Outline each Plasmodium ovale-infected red blood cell.
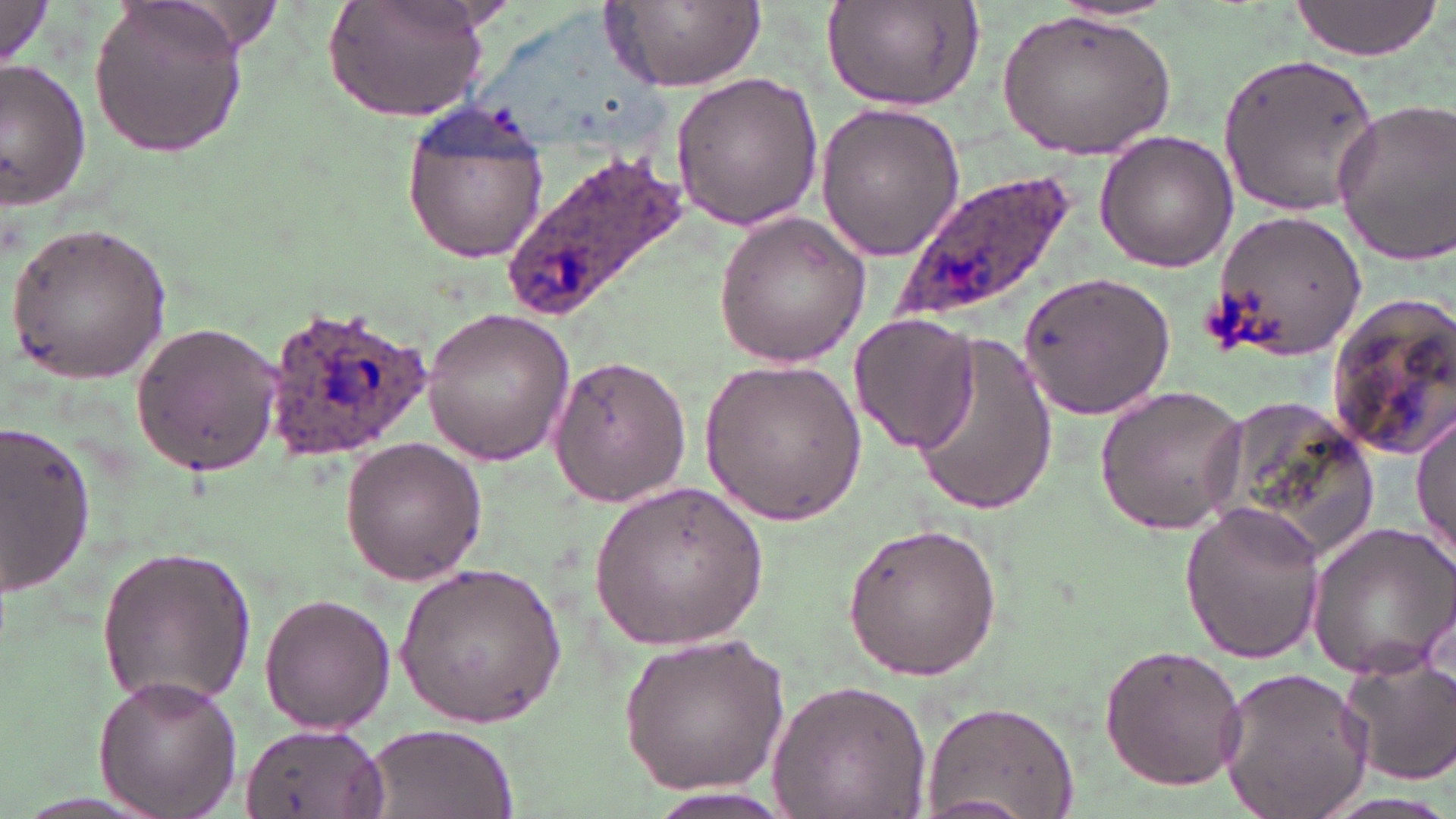
Approximate bounding boxes as named x1/y1/x2/y2 corners in pixels.
Plasmodium ovale-infected red blood cells: (x1=501, y1=145, x2=695, y2=321), (x1=897, y1=169, x2=1083, y2=323), (x1=265, y1=304, x2=434, y2=457).

Uninfected red blood cell locations: (x1=87, y1=0, x2=247, y2=160), (x1=323, y1=0, x2=492, y2=120), (x1=603, y1=0, x2=766, y2=92), (x1=1283, y1=0, x2=1445, y2=60), (x1=0, y1=2, x2=57, y2=72), (x1=821, y1=2, x2=985, y2=113), (x1=997, y1=10, x2=1176, y2=160), (x1=1216, y1=52, x2=1382, y2=215), (x1=0, y1=58, x2=92, y2=210), (x1=669, y1=70, x2=823, y2=231), (x1=1328, y1=97, x2=1456, y2=268), (x1=400, y1=101, x2=554, y2=266), (x1=813, y1=101, x2=967, y2=263), (x1=1093, y1=131, x2=1239, y2=273), (x1=1210, y1=209, x2=1368, y2=363), (x1=712, y1=211, x2=874, y2=368), (x1=5, y1=219, x2=171, y2=384), (x1=1017, y1=271, x2=1175, y2=422), (x1=1322, y1=292, x2=1456, y2=463), (x1=419, y1=306, x2=578, y2=465), (x1=849, y1=314, x2=980, y2=452), (x1=128, y1=320, x2=284, y2=479), (x1=907, y1=327, x2=1061, y2=526), (x1=548, y1=356, x2=693, y2=507), (x1=700, y1=356, x2=866, y2=529), (x1=1093, y1=383, x2=1249, y2=536), (x1=1194, y1=394, x2=1377, y2=567), (x1=1413, y1=411, x2=1455, y2=567), (x1=0, y1=422, x2=98, y2=597), (x1=340, y1=435, x2=486, y2=587), (x1=591, y1=480, x2=770, y2=648), (x1=1179, y1=500, x2=1324, y2=663), (x1=842, y1=520, x2=1001, y2=681), (x1=1306, y1=520, x2=1456, y2=683), (x1=92, y1=545, x2=259, y2=711), (x1=393, y1=563, x2=566, y2=729), (x1=257, y1=593, x2=398, y2=736), (x1=618, y1=629, x2=793, y2=794), (x1=1098, y1=643, x2=1248, y2=788), (x1=1339, y1=653, x2=1456, y2=786), (x1=1215, y1=667, x2=1374, y2=819), (x1=92, y1=676, x2=242, y2=816), (x1=769, y1=680, x2=931, y2=818), (x1=921, y1=699, x2=1082, y2=819), (x1=240, y1=723, x2=389, y2=819), (x1=364, y1=723, x2=517, y2=817), (x1=634, y1=785, x2=801, y2=819), (x1=1315, y1=792, x2=1456, y2=818). Slide-level diagnosis: Plasmodium ovale. Image is 1456×819 pixels. Captured at 1000x magnification. One field of a larger specimen. Optical microscopy. May-Grünwald-Giemsa-stained preparation. Thin blood film.